Assess this cell for malaria.
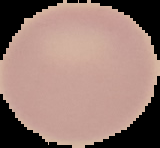

It is uninfected.

Segmented cell region on a black background. From a thin blood film. Image is 160×148 pixels.